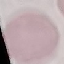
Summary:
  - Malaria status: uninfected
  - Image type: automatically extracted cell patch, resized to 64 × 64 pixels
  - Stain: Giemsa
  - Capture: smartphone through the microscope eyepiece
  - Preparation: thin smear